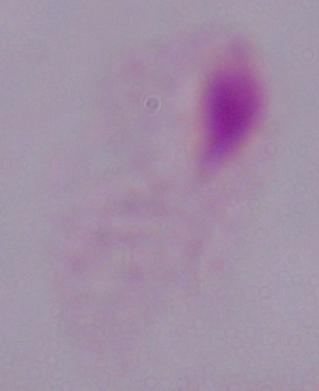
A trichomonad is shown. Captured at 1000x magnification. Photomicrograph.